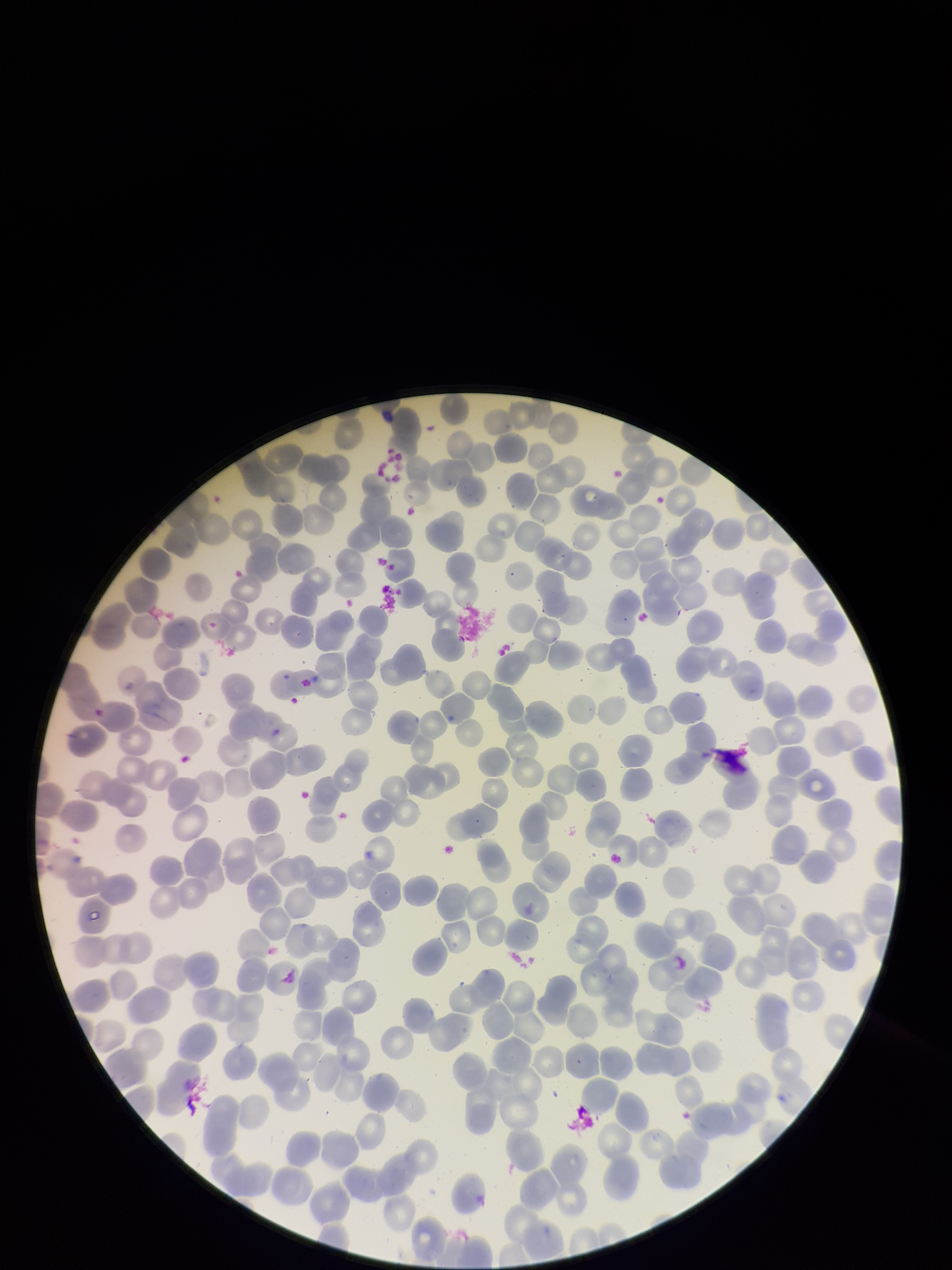 Parasitized red blood cell count: 0. Patient malaria status: negative. Image is 952×1270 pixels. Single field of view. Stained with Giemsa. Parasitized red blood cells: none seen. Red blood cell count: 286. Preparation: thin. Smartphone photograph taken through the eyepiece of a microscope.